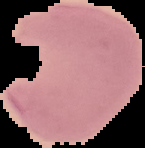

Summary:
  - Image type: segmented cell region on a black background
  - Image size: 145×148 pixels
  - Malaria status: parasitized
  - Preparation: thin blood smear